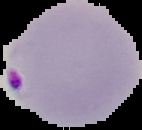
image_type: segmented cell region with the area outside set to black
image_size: 142×130 pixels
malaria_status: parasitized
preparation: thin blood film